Outline Plasmodium falciparum parasites and classify them by life-cycle stage.
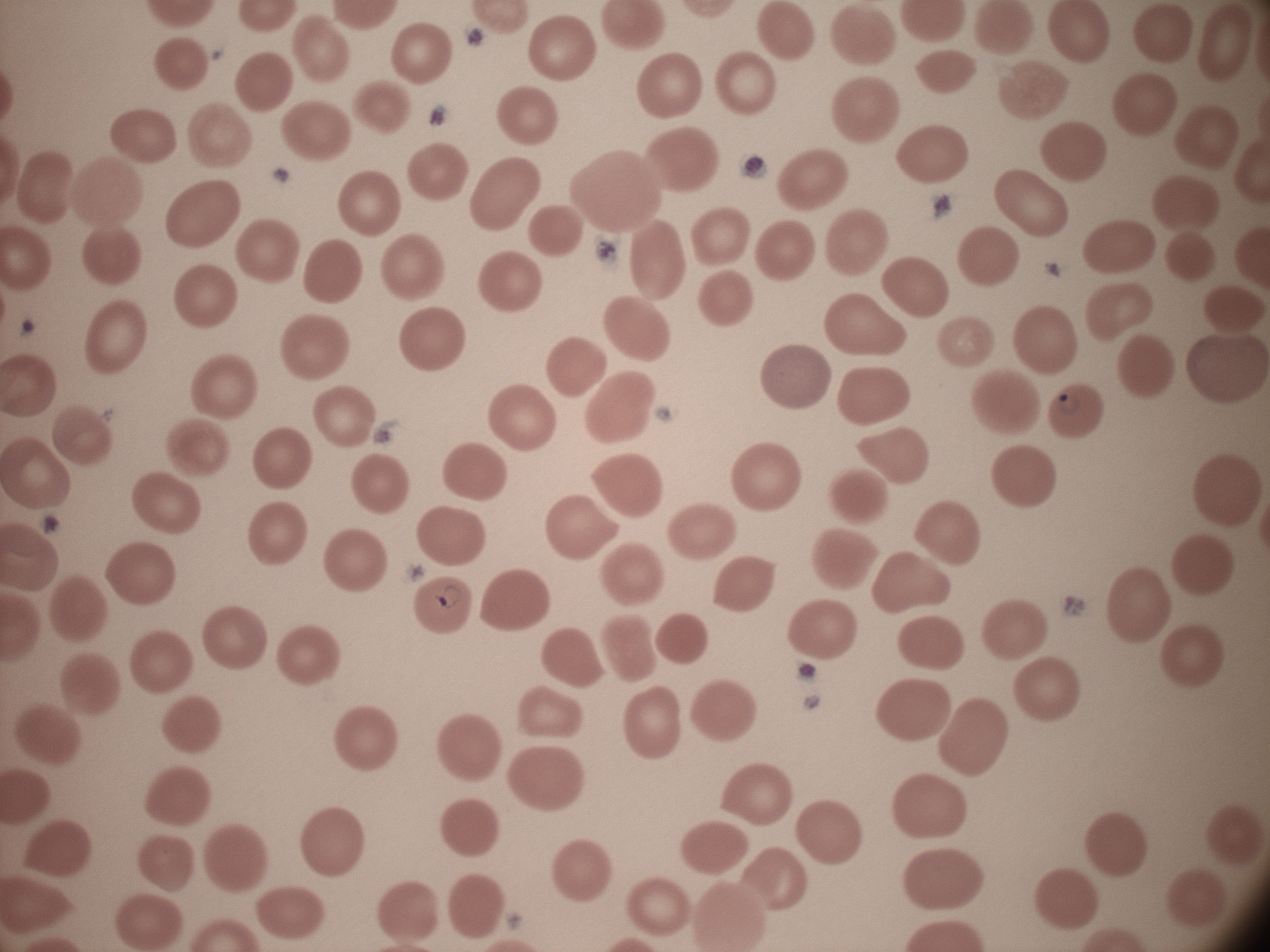

Approximate bounding boxes as named x1/y1/x2/y2 corners in pixels, from the source annotation, which is not necessarily exhaustive.
Ring forms: (x1=1053, y1=392, x2=1077, y2=415), (x1=433, y1=584, x2=463, y2=613).

Summary:
  - Magnification: 100x
  - Preparation: thin blood smear
  - Microscope: Leica DM2000 with built-in camera
  - Stain: Giemsa
  - Field of view: one from this slide
  - Image size: 1270×952 pixels
  - Species: Plasmodium falciparum